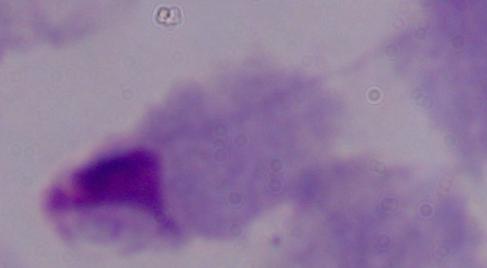

Summary:
  - Modality: micrograph
  - Identification: trichomonad
  - Magnification: 1000x